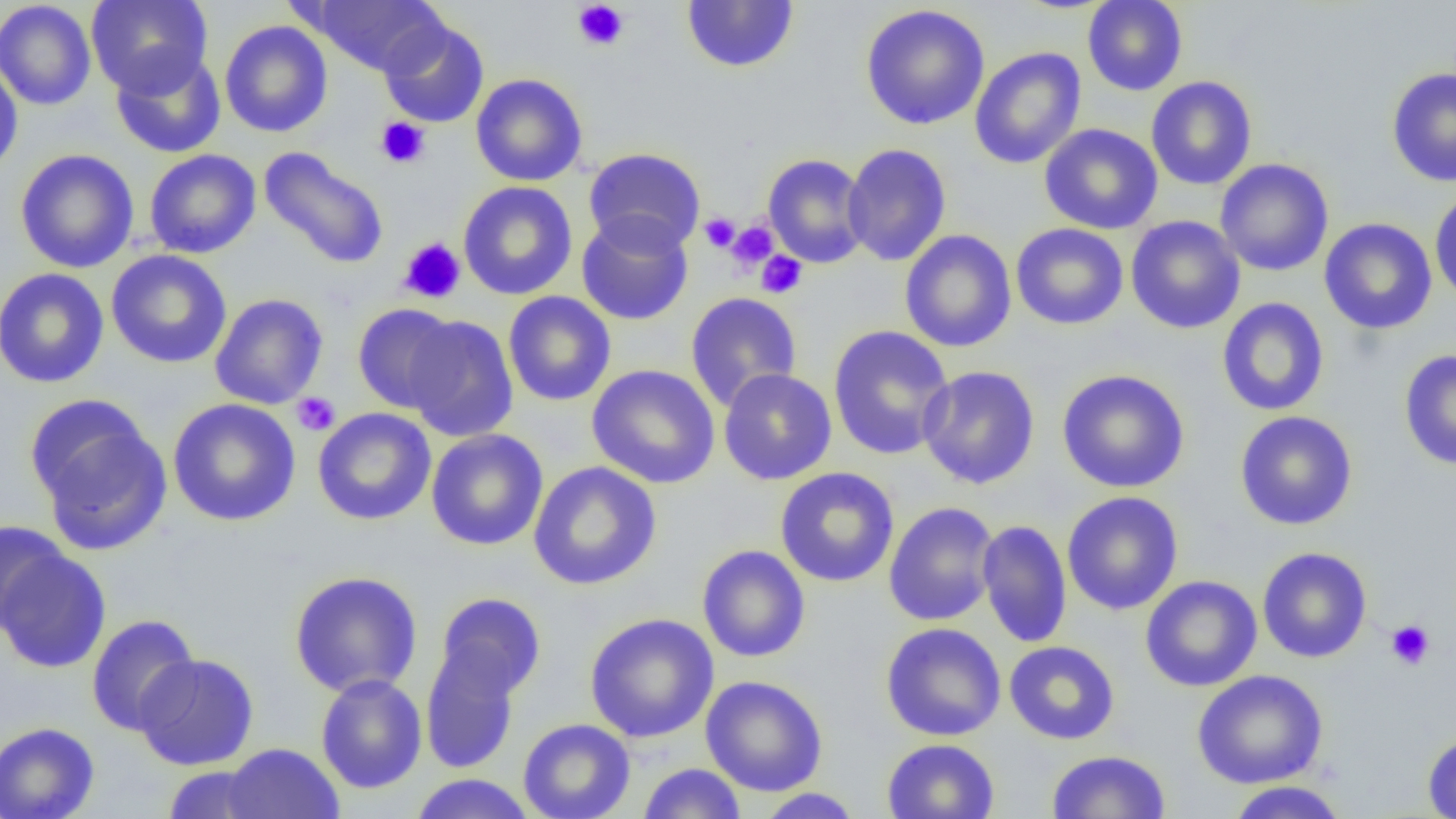

slide-level diagnosis = no evidence of blood parasites
image size = 1456×819 pixels
field of view = one of a larger specimen
modality = optical microscopy
preparation = thin blood smear
platelet locations = approximate bounding boxes as [x1, y1, x2, y2] in pixels: [571, 1, 629, 51], [375, 116, 430, 168], [699, 213, 740, 252], [726, 220, 780, 272], [397, 237, 466, 304], [756, 251, 808, 299], [292, 392, 341, 436], [1386, 620, 1435, 670]
magnification = 1000x
uninfected red blood cell locations = approximate bounding boxes as [x1, y1, x2, y2] in pixels: [86, 0, 212, 96], [308, 0, 446, 75], [1083, 0, 1188, 96], [0, 1, 97, 110], [682, 1, 799, 73], [860, 4, 990, 130], [378, 17, 489, 128], [219, 20, 333, 138], [969, 47, 1086, 170], [111, 48, 225, 159], [0, 59, 24, 178], [1386, 66, 1456, 187], [470, 73, 588, 186], [1145, 76, 1257, 190], [1039, 123, 1163, 235], [842, 143, 952, 266], [258, 147, 389, 270], [583, 147, 706, 255], [15, 149, 139, 273], [143, 149, 261, 259], [762, 153, 870, 268], [1215, 158, 1334, 277], [457, 181, 578, 300], [1430, 187, 1456, 306], [576, 212, 694, 326], [1125, 215, 1246, 334], [1319, 218, 1437, 335], [1010, 223, 1129, 330], [899, 230, 1017, 352], [105, 249, 232, 369], [0, 268, 110, 388], [503, 291, 616, 406], [685, 292, 803, 411], [210, 293, 329, 410], [1216, 297, 1330, 416], [352, 303, 464, 414], [403, 314, 519, 442], [828, 325, 955, 460], [1398, 348, 1456, 471], [586, 364, 720, 489], [917, 365, 1041, 490], [718, 368, 837, 485], [1057, 369, 1190, 493], [167, 398, 301, 526], [27, 399, 172, 556], [312, 407, 437, 525], [1234, 411, 1358, 531], [426, 429, 548, 551], [528, 461, 662, 590], [775, 467, 900, 587], [1062, 491, 1184, 615], [883, 501, 999, 626], [977, 519, 1072, 648], [0, 520, 70, 634], [697, 544, 811, 663], [1257, 546, 1372, 663], [0, 549, 111, 673], [288, 570, 423, 698], [1140, 575, 1262, 692], [434, 593, 547, 702], [584, 613, 719, 743], [86, 614, 200, 736], [880, 622, 1007, 741], [1004, 641, 1120, 745], [419, 643, 523, 774], [133, 653, 259, 770], [1191, 669, 1329, 789], [315, 674, 427, 794], [700, 675, 828, 797], [518, 718, 635, 819], [0, 722, 100, 819], [1422, 731, 1456, 819], [881, 738, 1000, 819], [221, 743, 344, 819], [1047, 750, 1170, 818], [637, 763, 747, 818], [161, 764, 270, 818], [410, 773, 536, 818], [1223, 781, 1352, 818], [754, 788, 865, 818]